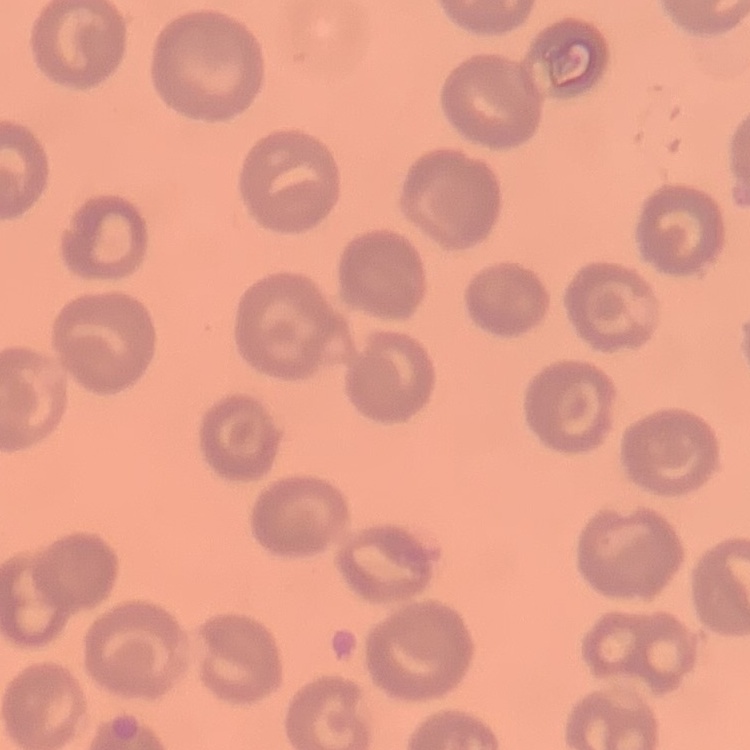
The erythrocytes show no rouleaux formation. Thin blood film. Square crop of a larger photomicrograph. Field's or Giemsa stain.